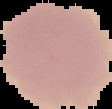
Malaria status: uninfected. From a thin blood smear. Segmented cell region on a black background. Image is 112×109 pixels.